Give the position of each P. falciparum parasite with its life-cycle stage, each leukocyte, and any debris.
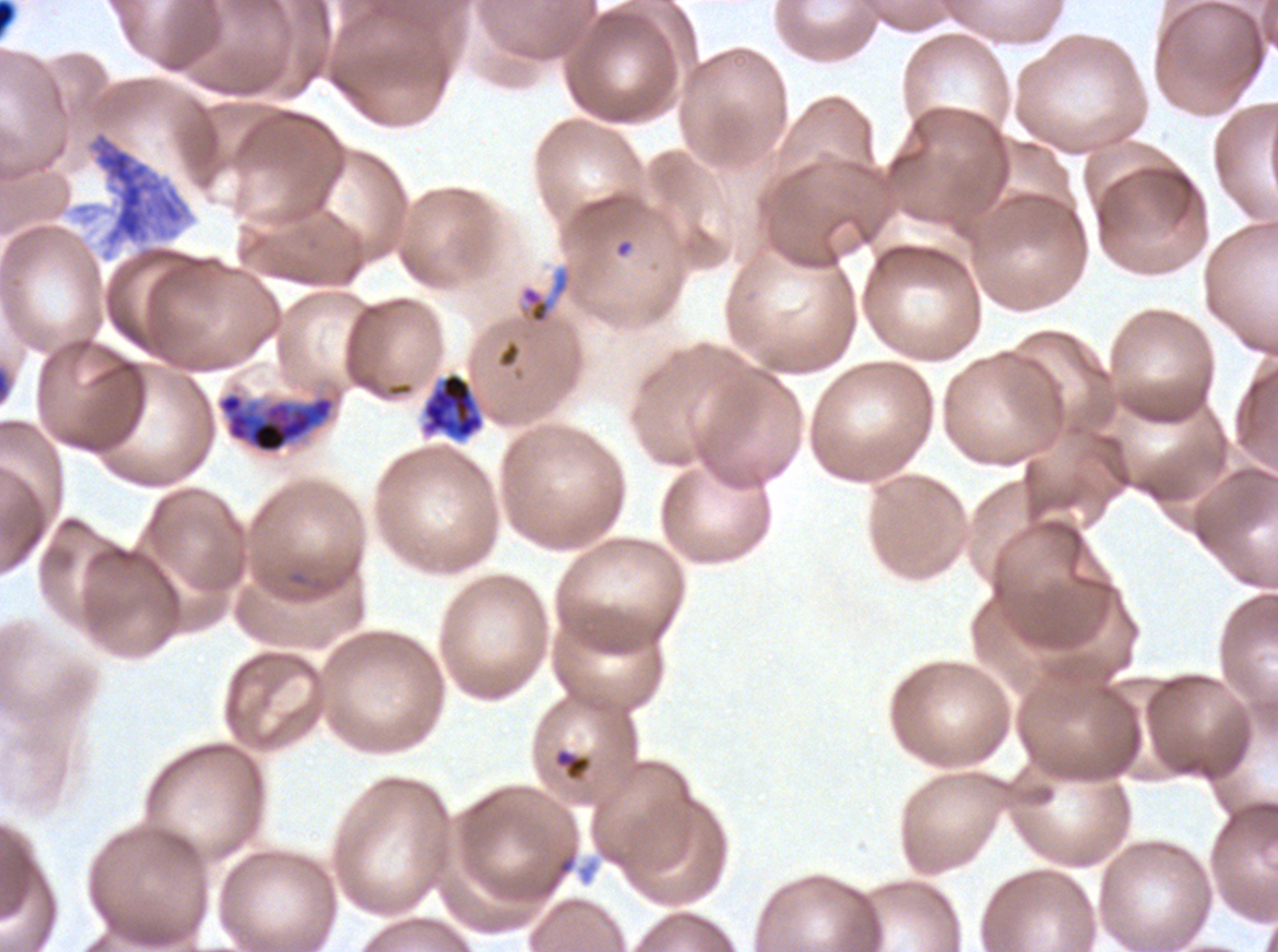

Approximate bounding boxes as {x1, y1, x2, y2} in pixels.
Late-ring/early-trophozoite forms: {553, 748, 592, 781}.
Mid trophozoites: {519, 267, 571, 325}.
Early schizonts: {217, 392, 336, 454}.
Segmenters: {421, 372, 485, 441}.
Debris: {87, 130, 190, 250}, {557, 857, 575, 875}.
No rings, late trophozoites, late schizonts, gametocytes, or leukocytes observed.

Summary:
  - Specimen: ex-vivo P. falciparum culture from a patient in The Gambia, grown for 24 to 48 hours
  - Stain: Giemsa
  - Field of view: sub-image separated from a larger composite
  - Preparation: thin blood smear
  - Life-cycle stages observed: late-ring/early-trophozoite, mid trophozoite, early schizont, segmenter
  - Image size: 1278×952 pixels